Describe the morphology of the red blood cells.
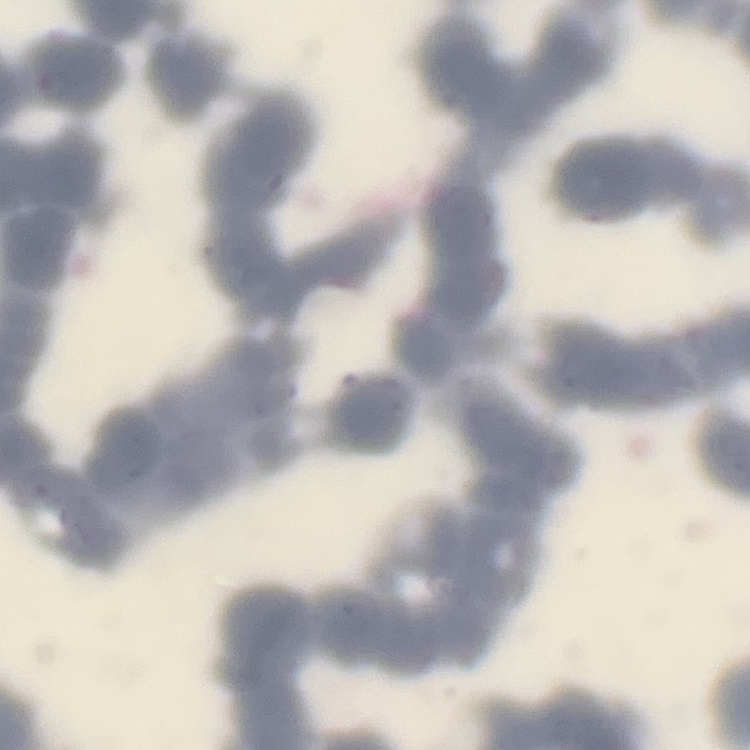

Rouleaux formation.

preparation = thin blood film
image type = one tile cut from a larger photomicrograph
stain = Field's or Giemsa